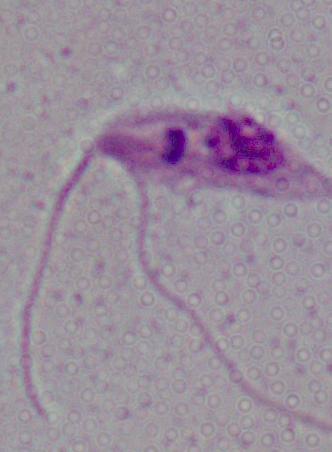
Summary:
  - Magnification: 1000x
  - Modality: micrograph
  - Identification: Leishmania